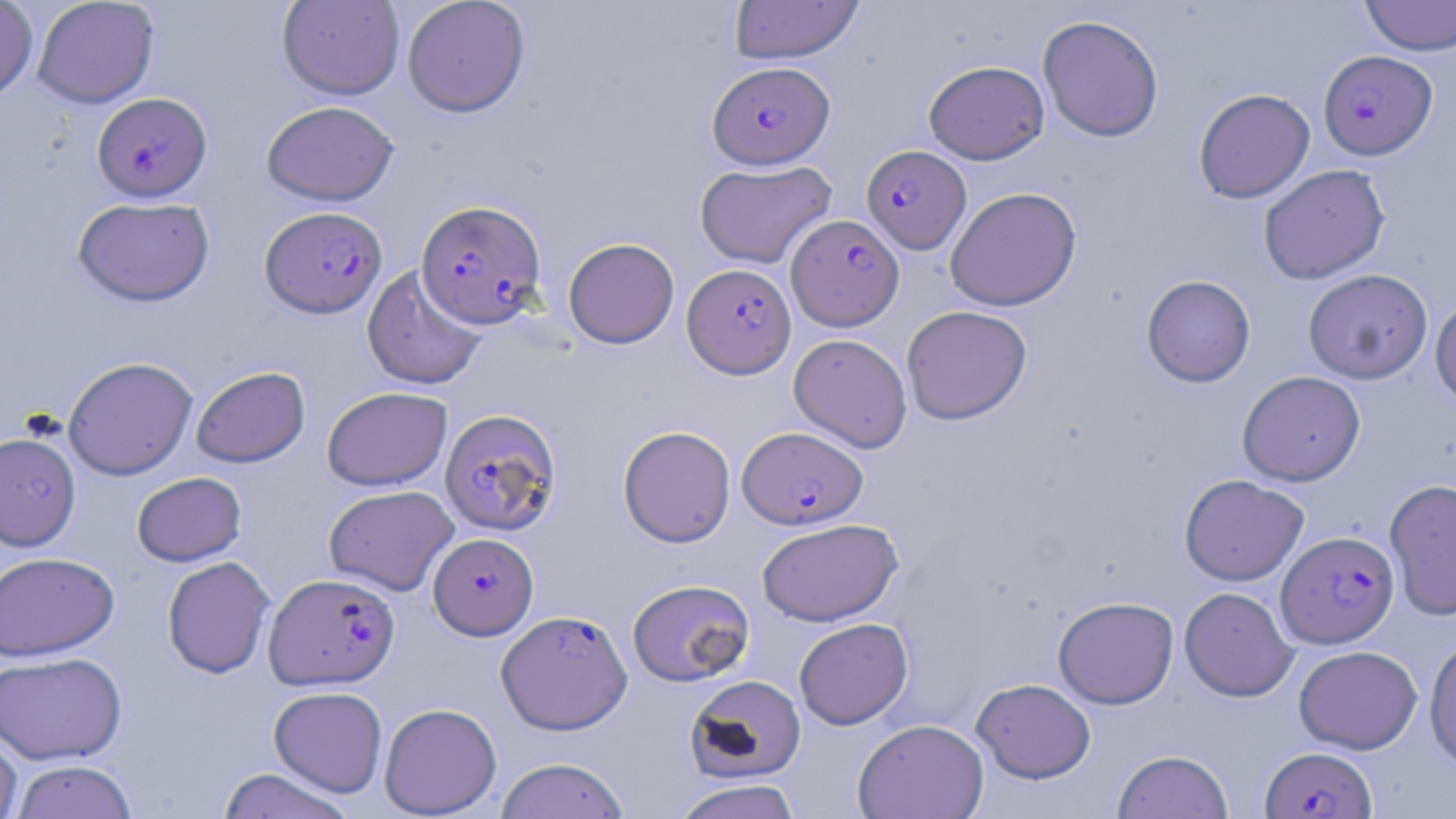
Summary:
  - Coordinate format: approximate bounding boxes as named x1/y1/x2/y2 corners in pixels
  - Uninfected red blood cell locations: (x1=0, y1=0, x2=38, y2=102), (x1=32, y1=0, x2=159, y2=108), (x1=277, y1=0, x2=405, y2=100), (x1=729, y1=0, x2=863, y2=64), (x1=1360, y1=0, x2=1456, y2=57), (x1=402, y1=1, x2=530, y2=117), (x1=1037, y1=14, x2=1164, y2=143), (x1=923, y1=60, x2=1049, y2=165), (x1=1193, y1=88, x2=1315, y2=204), (x1=261, y1=100, x2=398, y2=206), (x1=695, y1=160, x2=836, y2=269), (x1=1258, y1=164, x2=1390, y2=285), (x1=944, y1=187, x2=1082, y2=311), (x1=72, y1=196, x2=215, y2=307), (x1=563, y1=237, x2=680, y2=348), (x1=362, y1=265, x2=488, y2=391), (x1=1303, y1=268, x2=1433, y2=384), (x1=1141, y1=274, x2=1256, y2=387), (x1=1430, y1=295, x2=1456, y2=409), (x1=901, y1=305, x2=1032, y2=425), (x1=788, y1=334, x2=912, y2=453), (x1=62, y1=356, x2=198, y2=480), (x1=191, y1=366, x2=310, y2=468), (x1=1237, y1=371, x2=1365, y2=486), (x1=321, y1=386, x2=452, y2=491), (x1=618, y1=425, x2=736, y2=547), (x1=0, y1=432, x2=81, y2=552), (x1=131, y1=472, x2=247, y2=567), (x1=1179, y1=474, x2=1308, y2=586), (x1=1384, y1=478, x2=1456, y2=622), (x1=323, y1=485, x2=459, y2=596), (x1=757, y1=518, x2=902, y2=626), (x1=0, y1=551, x2=119, y2=661), (x1=162, y1=556, x2=274, y2=679), (x1=627, y1=579, x2=754, y2=686), (x1=1179, y1=587, x2=1298, y2=702), (x1=1053, y1=596, x2=1178, y2=708), (x1=794, y1=618, x2=912, y2=729), (x1=1424, y1=637, x2=1456, y2=770), (x1=1294, y1=645, x2=1423, y2=754), (x1=0, y1=651, x2=126, y2=765), (x1=685, y1=675, x2=806, y2=783), (x1=971, y1=678, x2=1096, y2=783), (x1=268, y1=686, x2=388, y2=797), (x1=379, y1=702, x2=502, y2=817), (x1=853, y1=718, x2=989, y2=819), (x1=0, y1=729, x2=22, y2=819), (x1=1112, y1=749, x2=1234, y2=819), (x1=494, y1=757, x2=630, y2=818), (x1=10, y1=759, x2=139, y2=819), (x1=217, y1=767, x2=357, y2=819), (x1=672, y1=778, x2=802, y2=819)
  - Plasmodium falciparum-infected red blood cell locations: (x1=1318, y1=50, x2=1437, y2=160), (x1=708, y1=61, x2=835, y2=168), (x1=93, y1=92, x2=212, y2=201), (x1=861, y1=144, x2=971, y2=253), (x1=416, y1=200, x2=547, y2=328), (x1=260, y1=206, x2=387, y2=318), (x1=786, y1=214, x2=904, y2=331), (x1=682, y1=263, x2=796, y2=378), (x1=439, y1=408, x2=562, y2=536), (x1=737, y1=426, x2=867, y2=529), (x1=1276, y1=531, x2=1399, y2=648), (x1=428, y1=532, x2=538, y2=639), (x1=264, y1=572, x2=400, y2=690), (x1=496, y1=609, x2=632, y2=734), (x1=1260, y1=745, x2=1376, y2=819)
  - Slide-level diagnosis: Plasmodium falciparum
  - Stain: May-Grünwald-Giemsa
  - Modality: light microscopy
  - Image size: 1456×819 pixels
  - Preparation: thin blood smear
  - Magnification: 1000x
  - Field of view: one of a larger specimen